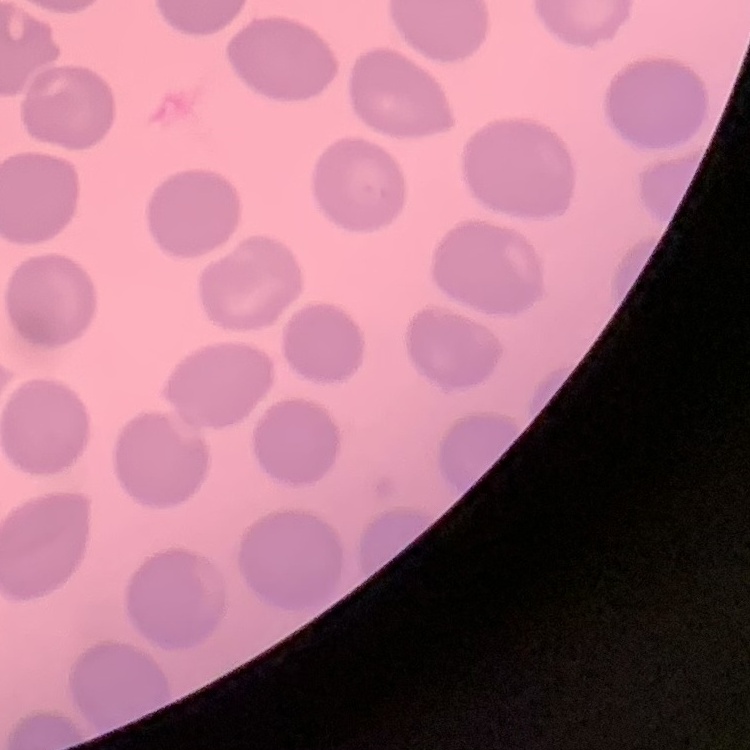

red blood cell morphology = no rouleaux formation
stain = Field's or Giemsa
preparation = thin blood film
image type = square crop of a larger photomicrograph